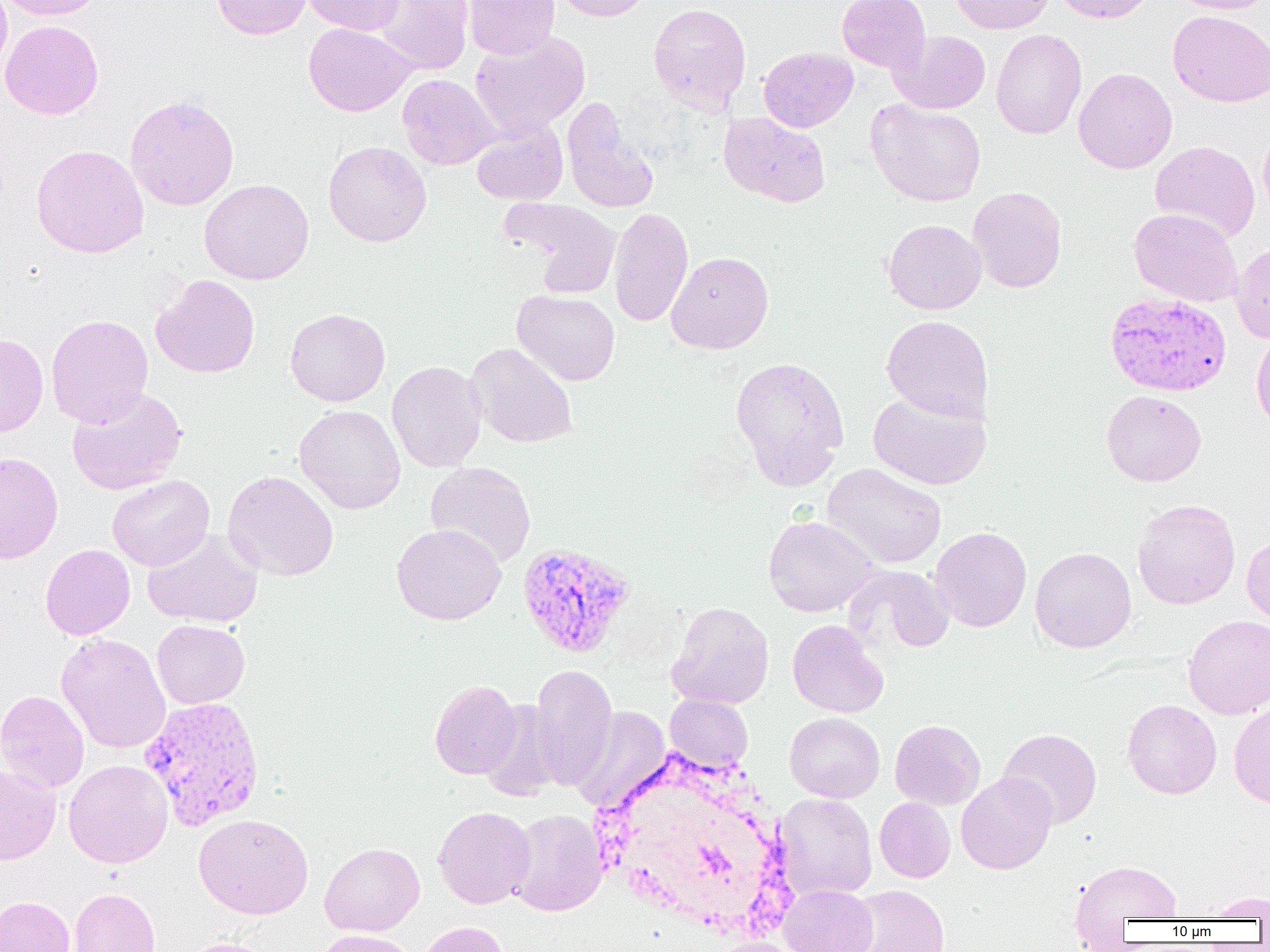

{
  "slide_level_diagnosis": "Plasmodium vivax",
  "field_of_view": "one of a larger specimen",
  "plasmodium_vivax_infected_red_blood_cell_locations": "approximate bounding boxes as [x1, y1, x2, y2] in pixels: [1104, 292, 1232, 397], [516, 542, 636, 658], [139, 694, 266, 832]",
  "modality": "optical microscopy",
  "image_size": "1270×952 pixels",
  "uninfected_red_blood_cell_locations": "approximate bounding boxes as [x1, y1, x2, y2] in pixels: [1, 0, 108, 21], [211, 0, 312, 40], [301, 0, 406, 35], [372, 0, 474, 75], [463, 0, 559, 60], [552, 0, 655, 22], [837, 0, 930, 73], [950, 0, 1054, 34], [1053, 0, 1157, 24], [1170, 0, 1270, 14], [0, 1, 12, 80], [648, 2, 751, 114], [1168, 11, 1270, 107], [1, 20, 104, 120], [304, 23, 416, 116], [990, 29, 1087, 139], [470, 30, 590, 138], [892, 31, 990, 114], [758, 47, 858, 132], [1074, 67, 1177, 173], [397, 74, 499, 170], [125, 94, 239, 211], [561, 98, 659, 213], [866, 99, 986, 207], [719, 111, 831, 208], [471, 120, 568, 205], [1257, 121, 1270, 226], [323, 141, 431, 247], [1149, 141, 1261, 243], [31, 144, 149, 259], [199, 178, 314, 285], [967, 186, 1067, 293], [500, 198, 621, 296], [609, 206, 693, 327], [1129, 208, 1243, 307], [883, 219, 986, 314], [1231, 240, 1270, 343], [666, 251, 774, 354], [151, 275, 260, 378], [512, 289, 620, 386], [285, 308, 390, 406], [46, 314, 153, 428], [881, 314, 994, 423], [1251, 328, 1270, 433], [0, 332, 49, 438], [466, 342, 578, 448], [730, 355, 850, 489], [386, 360, 487, 473], [66, 387, 188, 495], [869, 389, 990, 490], [1101, 390, 1206, 486], [294, 404, 406, 514], [0, 452, 63, 563], [425, 461, 536, 568], [823, 462, 947, 569], [223, 470, 339, 581], [107, 475, 214, 570], [1132, 498, 1241, 610], [763, 515, 881, 617], [391, 523, 506, 625], [930, 526, 1032, 632], [142, 529, 263, 628], [1241, 534, 1270, 624], [40, 544, 135, 640], [1030, 547, 1136, 653], [845, 566, 955, 654], [666, 600, 775, 709], [1183, 614, 1270, 718], [152, 619, 250, 709], [788, 620, 888, 718], [56, 633, 171, 754], [529, 664, 618, 789], [429, 679, 522, 779], [1, 690, 89, 793], [665, 694, 753, 772], [1122, 699, 1222, 799], [1228, 699, 1270, 810], [479, 701, 566, 800], [573, 706, 670, 812], [785, 712, 885, 803], [890, 719, 985, 810], [998, 728, 1102, 829], [64, 759, 173, 868], [0, 765, 61, 865], [956, 773, 1056, 874], [776, 793, 877, 900], [875, 797, 955, 882], [433, 806, 535, 909], [508, 809, 607, 916], [192, 813, 313, 919], [320, 842, 424, 936], [1070, 860, 1182, 930], [780, 884, 877, 952], [844, 885, 950, 952], [69, 887, 161, 952], [1201, 891, 1270, 920], [0, 896, 75, 952], [415, 920, 511, 952], [316, 929, 417, 952], [711, 936, 801, 952], [176, 937, 275, 952]",
  "white_blood_cell_locations": "approximate bounding boxes as [x1, y1, x2, y2] in pixels: [588, 746, 802, 943]",
  "preparation": "thin blood smear",
  "magnification": "1000x"
}